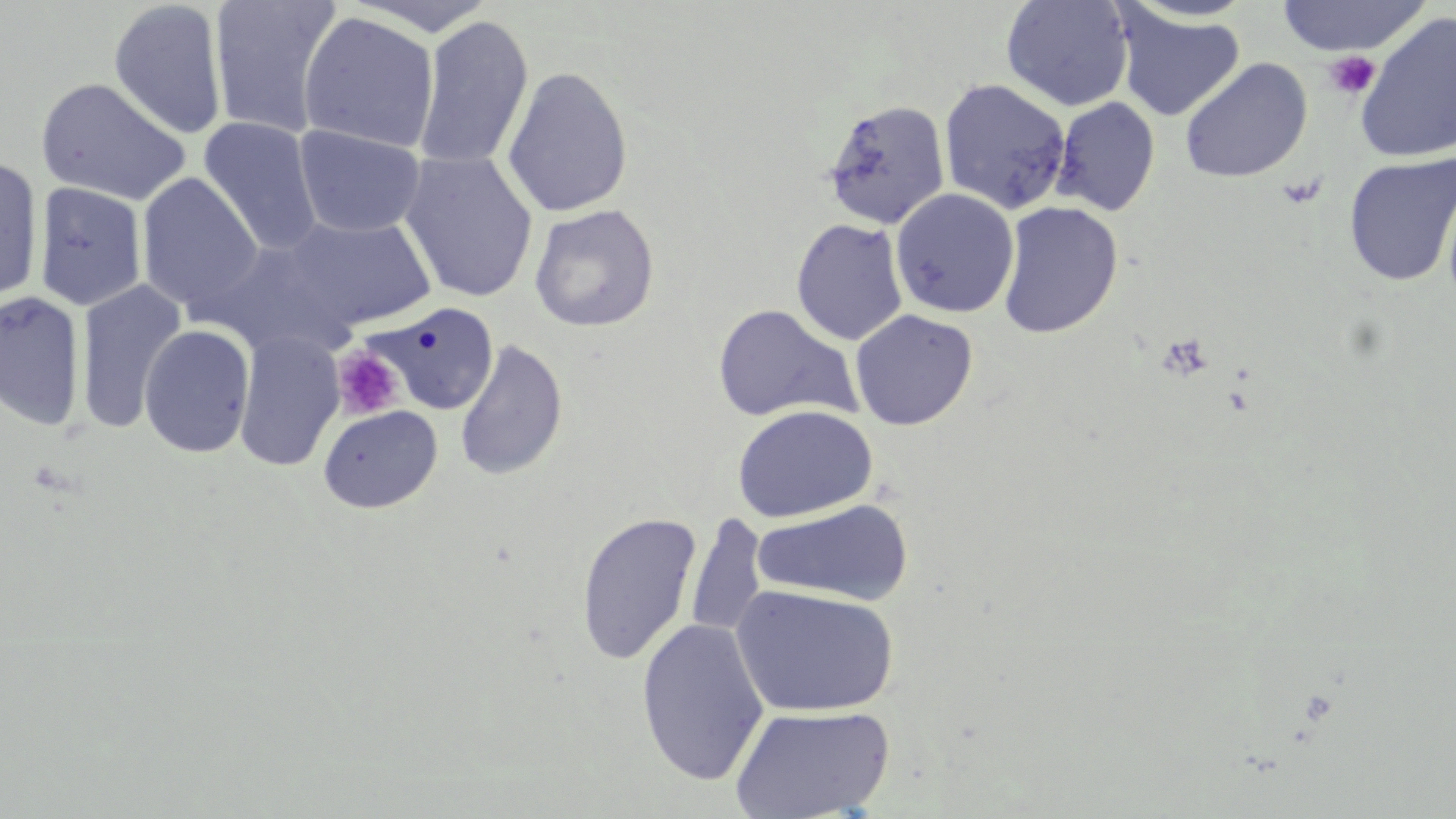
Summary:
  - Coordinate format: approximate bounding boxes as (x1,y1)-(x2,y2) corner pairs in pixels
  - Uninfected red blood cell locations: (207,0)-(342,140), (343,0)-(500,36), (1001,0)-(1135,112), (1275,0)-(1430,57), (107,2)-(228,140), (1113,6)-(1245,122), (1354,10)-(1456,165), (298,11)-(440,154), (414,14)-(534,172), (1180,57)-(1312,183), (501,65)-(633,218), (36,77)-(191,206), (938,79)-(1072,215), (1052,98)-(1161,216), (823,100)-(950,229), (197,117)-(323,256), (293,124)-(427,238), (397,151)-(538,304), (1343,152)-(1456,287), (0,155)-(44,309), (136,173)-(263,313), (32,182)-(148,311), (890,189)-(1019,318), (997,201)-(1124,338), (528,204)-(660,333), (282,214)-(437,332), (791,218)-(909,345), (210,239)-(354,357), (75,279)-(187,434), (0,290)-(85,432), (363,301)-(500,415), (711,304)-(861,424), (850,309)-(978,431), (139,323)-(256,458), (233,329)-(345,472), (454,339)-(569,482), (318,404)-(443,514), (732,404)-(878,524), (750,498)-(914,608), (574,511)-(703,666), (685,515)-(768,643), (731,584)-(898,718), (636,618)-(770,787), (730,704)-(894,818)
  - Platelet locations: (1323,50)-(1380,99), (1279,173)-(1325,209), (332,346)-(404,420)
  - Slide-level diagnosis: no evidence of blood parasites
  - Modality: light microscopy
  - Stain: May-Grünwald-Giemsa
  - Preparation: thin blood film
  - Image size: 1456×819 pixels
  - Magnification: 1000x
  - Field of view: one of a larger specimen